Locate every blood parasite and identify its species.
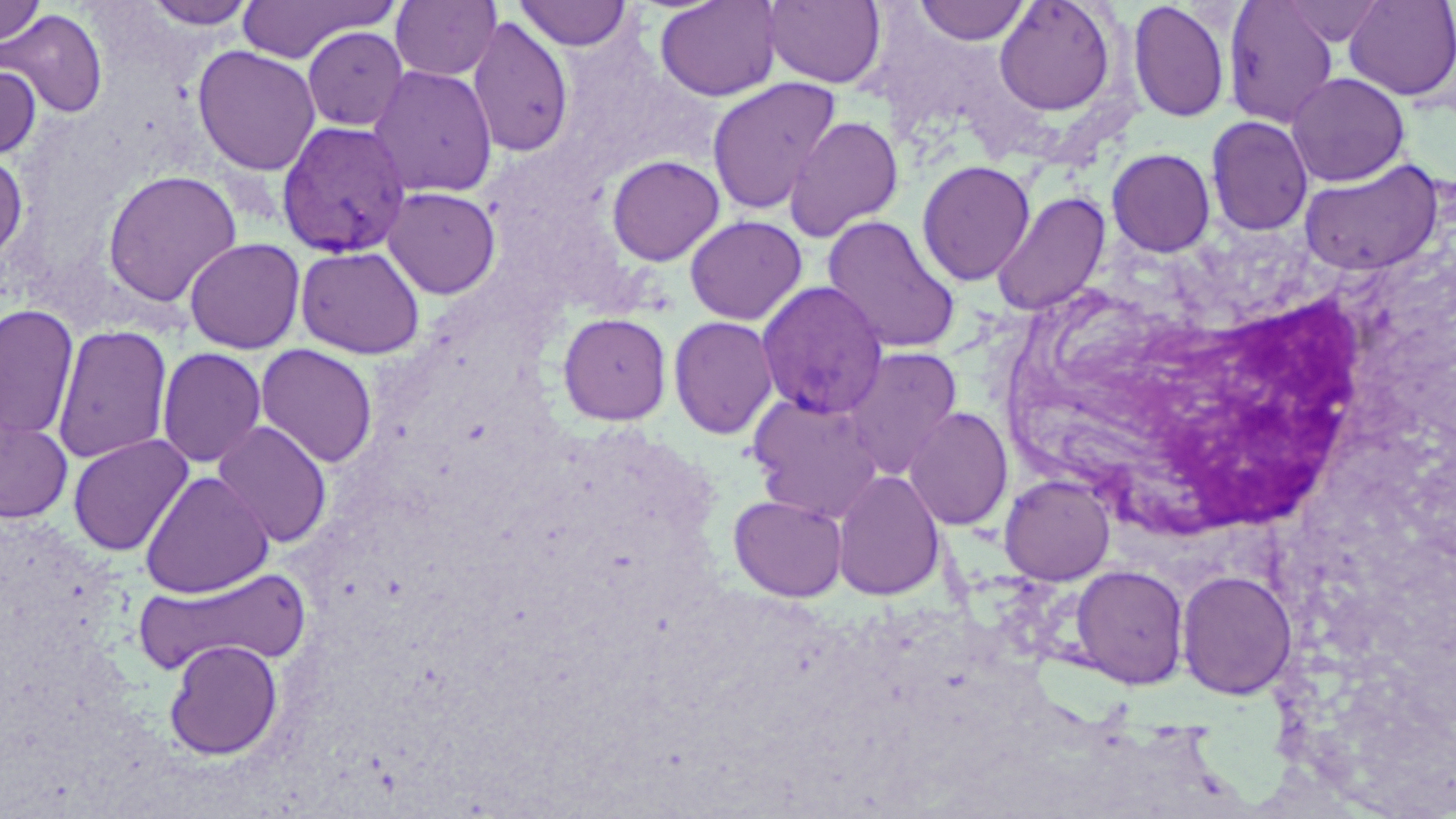
Approximate bounding boxes as (x1,y1)-(x2,y2) corner pairs in pixels.
Plasmodium vivax-infected red blood cells: (276,120)-(411,258), (756,281)-(888,419).
No Plasmodium falciparum, Plasmodium ovale, Plasmodium malariae, Babesia divergens, or Trypanosoma brucei observed.

White blood cell locations: (1137,287)-(1378,544). Uninfected red blood cell locations: (141,0)-(258,29), (236,0)-(392,64), (654,0)-(782,102), (763,0)-(887,88), (995,0)-(1118,117), (1223,0)-(1340,128), (1278,0)-(1387,46), (1343,0)-(1456,101), (390,1)-(501,82), (514,1)-(635,51), (914,1)-(1030,45), (1128,1)-(1230,123), (0,2)-(46,45), (1,8)-(108,119), (467,16)-(574,158), (302,26)-(409,132), (193,45)-(321,176), (0,62)-(41,161), (368,65)-(498,199), (1287,72)-(1409,186), (706,77)-(841,215), (783,115)-(904,242), (1206,115)-(1314,237), (1107,148)-(1215,257), (0,151)-(28,268), (606,154)-(725,266), (1298,158)-(1444,277), (917,160)-(1036,286), (102,169)-(242,307), (382,187)-(501,298), (990,191)-(1110,317), (684,215)-(806,325), (822,215)-(961,354), (183,237)-(305,354), (295,245)-(425,359), (1,304)-(79,440), (558,312)-(672,425), (668,316)-(779,439), (51,323)-(173,464), (255,344)-(378,468), (156,347)-(267,468), (841,347)-(963,479), (748,393)-(885,521), (903,406)-(1013,531), (0,415)-(73,524), (212,421)-(332,548), (67,434)-(194,556), (831,469)-(946,601), (139,470)-(274,598), (999,474)-(1115,585), (729,495)-(847,602), (1070,564)-(1189,689), (135,567)-(311,674), (1176,569)-(1297,700), (164,639)-(283,760). Slide-level diagnosis: Plasmodium vivax. Optical microscopy. May-Grünwald-Giemsa-stained preparation. Captured at 1000x magnification. Thin blood film. One field of a larger specimen. Image is 1456×819 pixels.